Identify the parasite.
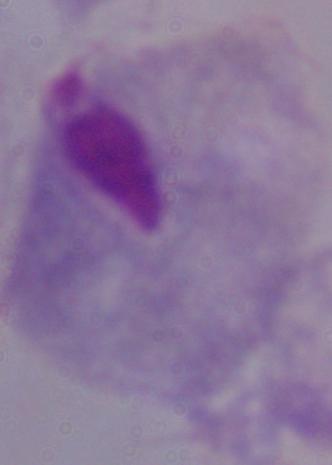
This is a trichomonad.

1000x magnification. Micrograph.